Locate every blood parasite and identify its species.
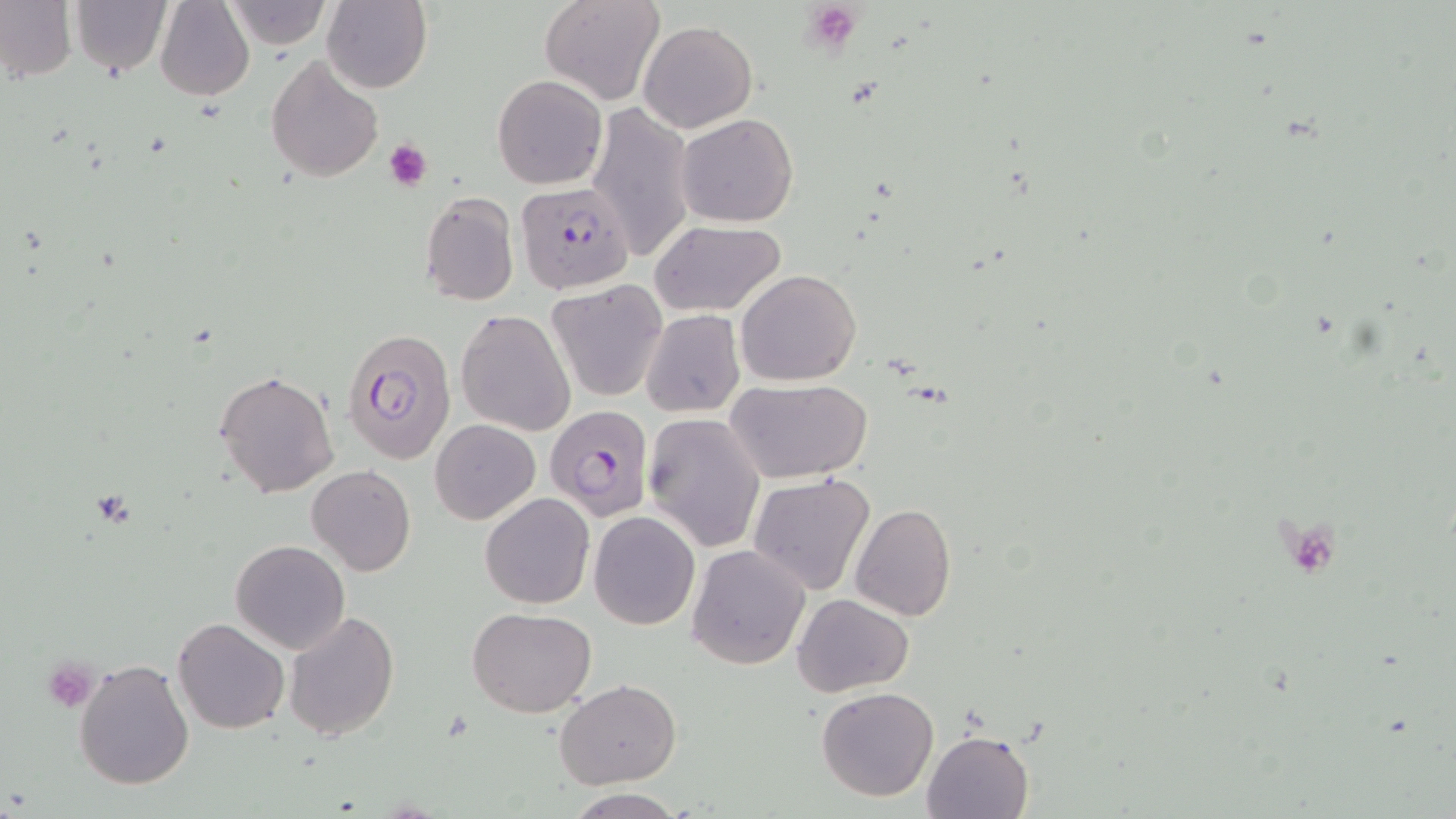

Approximate bounding boxes as named x1/y1/x2/y2 corners in pixels.
Plasmodium falciparum-infected red blood cells: (x1=513, y1=182, x2=635, y2=296), (x1=343, y1=326, x2=457, y2=465), (x1=544, y1=402, x2=653, y2=520).
No Plasmodium ovale, Plasmodium malariae, Plasmodium vivax, Babesia divergens, or Trypanosoma brucei observed.

Platelet locations: (x1=800, y1=1, x2=865, y2=55), (x1=383, y1=138, x2=434, y2=190), (x1=42, y1=658, x2=99, y2=712). Uninfected red blood cell locations: (x1=0, y1=0, x2=77, y2=83), (x1=68, y1=0, x2=172, y2=76), (x1=154, y1=0, x2=254, y2=101), (x1=321, y1=0, x2=432, y2=95), (x1=539, y1=0, x2=666, y2=106), (x1=224, y1=1, x2=331, y2=50), (x1=639, y1=19, x2=757, y2=132), (x1=266, y1=53, x2=384, y2=183), (x1=493, y1=75, x2=607, y2=190), (x1=587, y1=104, x2=696, y2=263), (x1=676, y1=113, x2=798, y2=225), (x1=419, y1=192, x2=519, y2=308), (x1=649, y1=220, x2=786, y2=317), (x1=735, y1=270, x2=860, y2=386), (x1=546, y1=281, x2=668, y2=401), (x1=456, y1=309, x2=577, y2=436), (x1=642, y1=309, x2=745, y2=418), (x1=214, y1=369, x2=340, y2=500), (x1=725, y1=378, x2=873, y2=483), (x1=642, y1=412, x2=765, y2=553), (x1=430, y1=419, x2=540, y2=523), (x1=306, y1=465, x2=416, y2=576), (x1=748, y1=472, x2=875, y2=595), (x1=480, y1=493, x2=595, y2=609), (x1=850, y1=503, x2=957, y2=621), (x1=589, y1=511, x2=700, y2=629), (x1=230, y1=539, x2=351, y2=654), (x1=687, y1=544, x2=810, y2=670), (x1=793, y1=593, x2=914, y2=698), (x1=468, y1=606, x2=596, y2=717), (x1=282, y1=608, x2=399, y2=741), (x1=172, y1=616, x2=289, y2=734), (x1=74, y1=658, x2=195, y2=790), (x1=555, y1=680, x2=680, y2=788), (x1=816, y1=686, x2=939, y2=802), (x1=922, y1=730, x2=1034, y2=819), (x1=564, y1=790, x2=688, y2=819). Slide-level diagnosis: Plasmodium falciparum. Thin blood film. May-Grünwald-Giemsa stain. Image is 1456×819 pixels. Captured at 1000x magnification. Light microscopy. Single field of view.